Name the parasite shown.
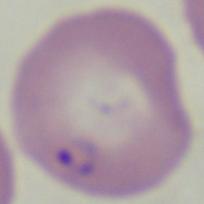

Babesia.

modality = micrograph
magnification = 1000x